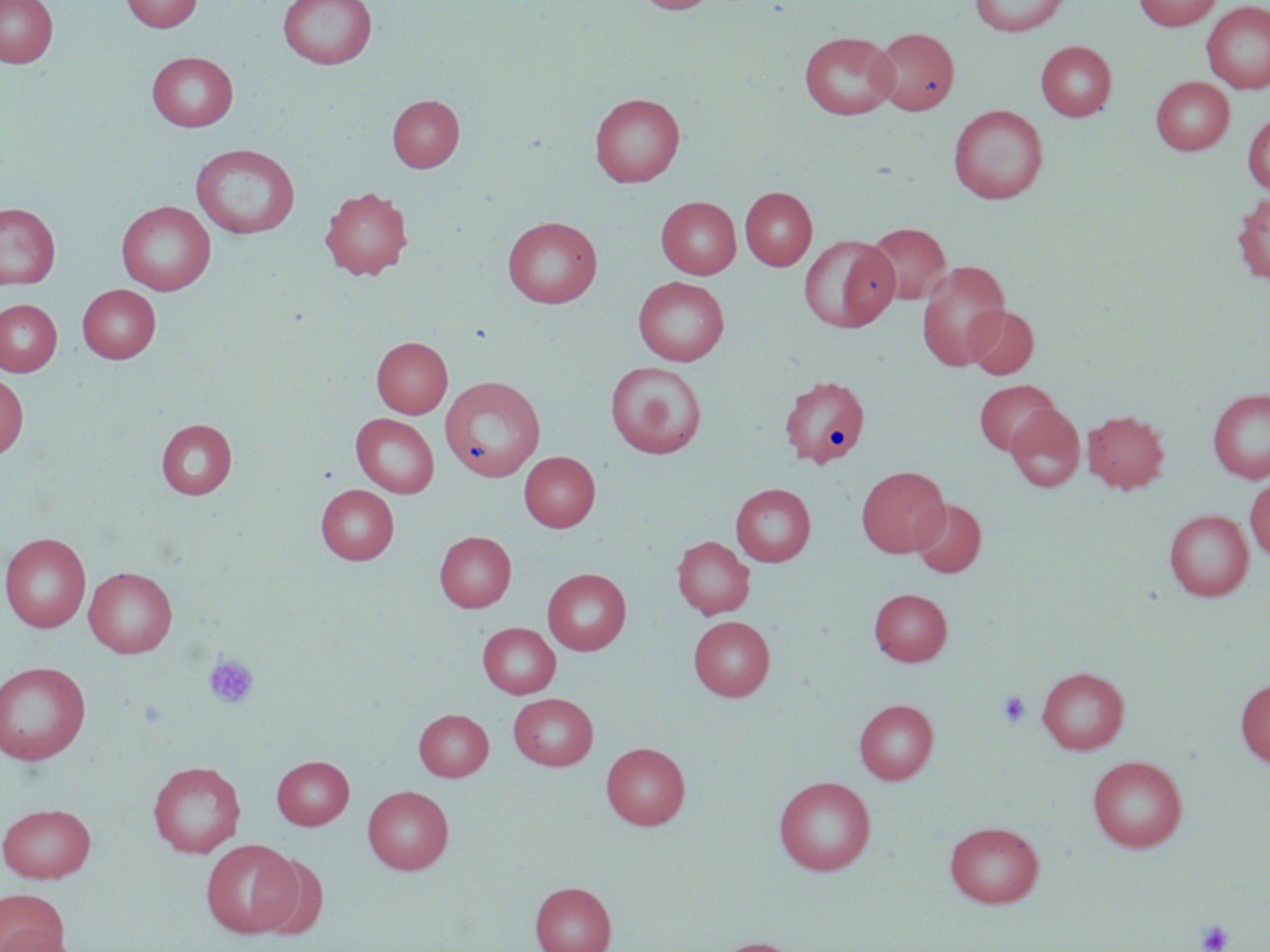
Approximate bounding boxes as [x1, y1, x2, y2] in pixels. Platelet locations: [203, 654, 260, 709], [998, 691, 1031, 727], [1196, 919, 1234, 952]. Uninfected red blood cell locations: [0, 0, 58, 67], [122, 0, 202, 33], [277, 0, 377, 70], [632, 0, 718, 14], [969, 0, 1071, 36], [1133, 0, 1223, 30], [1201, 1, 1270, 94], [871, 27, 959, 115], [798, 31, 900, 120], [1036, 41, 1116, 121], [147, 51, 239, 132], [1151, 77, 1234, 154], [589, 92, 684, 187], [387, 94, 464, 172], [947, 104, 1048, 204], [1243, 110, 1270, 196], [190, 144, 300, 239], [320, 186, 413, 279], [740, 187, 817, 270], [1232, 192, 1270, 286], [656, 196, 741, 278], [117, 200, 216, 295], [0, 202, 61, 289], [502, 216, 603, 308], [864, 223, 951, 306], [799, 235, 899, 333], [916, 261, 1010, 371], [633, 276, 729, 366], [78, 284, 161, 362], [0, 299, 62, 376], [964, 305, 1038, 379], [371, 336, 452, 418], [605, 361, 707, 459], [0, 373, 28, 459], [779, 375, 870, 468], [974, 380, 1060, 455], [435, 381, 543, 482], [1208, 388, 1270, 483], [1005, 404, 1085, 492], [1082, 408, 1170, 493], [351, 413, 439, 497], [156, 418, 237, 499], [519, 451, 600, 531], [856, 465, 949, 557], [1245, 478, 1270, 561], [731, 483, 816, 566], [316, 484, 398, 563], [910, 499, 986, 577], [1164, 509, 1253, 600], [434, 530, 516, 612], [1, 533, 91, 632], [672, 536, 755, 618], [84, 566, 177, 657], [542, 568, 631, 654], [869, 587, 952, 666], [689, 616, 774, 700], [478, 622, 560, 698], [0, 661, 91, 764], [1037, 666, 1129, 753], [1235, 678, 1270, 768], [508, 693, 598, 770], [854, 698, 938, 784], [414, 709, 493, 781], [601, 741, 690, 829], [272, 755, 354, 829], [1088, 755, 1188, 852], [148, 760, 246, 858], [774, 776, 875, 875], [363, 785, 454, 874], [0, 802, 96, 883], [945, 821, 1044, 908], [201, 839, 301, 938], [254, 853, 329, 940], [531, 881, 616, 952], [0, 888, 69, 952], [1, 929, 84, 951], [709, 937, 805, 952]. Slide-level diagnosis: no evidence of blood parasites. Captured at 1000x magnification. Image is 1270×952 pixels. Thin blood smear. May-Grünwald-Giemsa stain. Optical microscopy. One field of a larger specimen.